Evaluate for Plasmodium parasites.
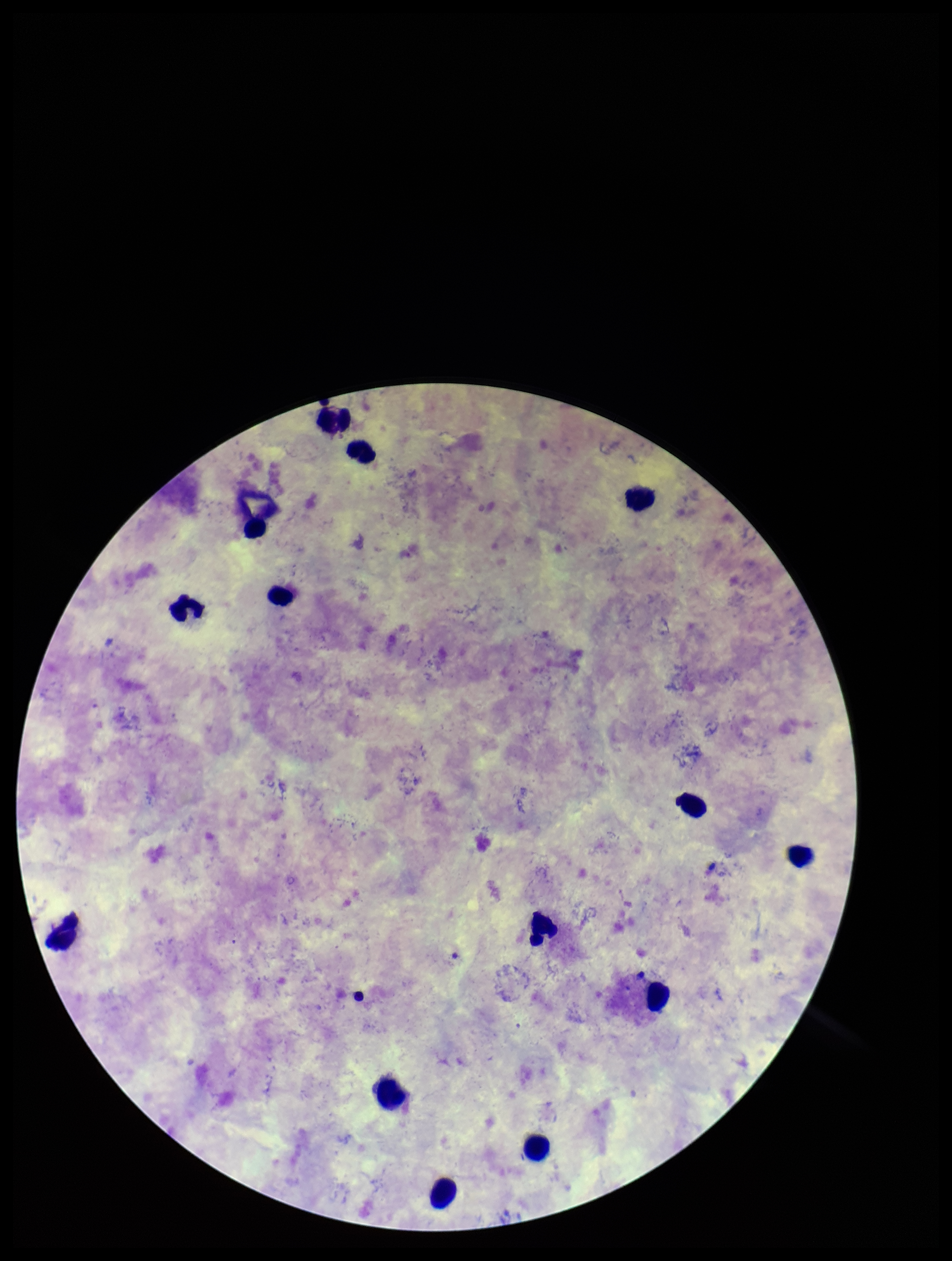
None identified.

capture: smartphone photograph through the microscope eyepiece
preparation: thick smear
field_of_view: one from this slide
stain: Giemsa
image_size: 952×1261 pixels
patient_malaria_status: positive
parasite_count: 0
species_reported_for_this_patient: Plasmodium vivax
leukocyte_count: 14